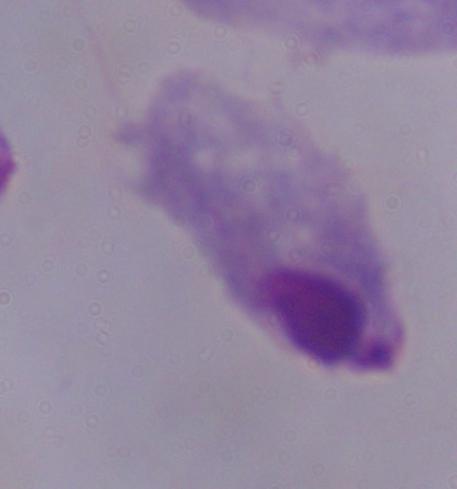
A trichomonad is shown. Micrograph. Captured at 1000x magnification.